Name the blood parasite species.
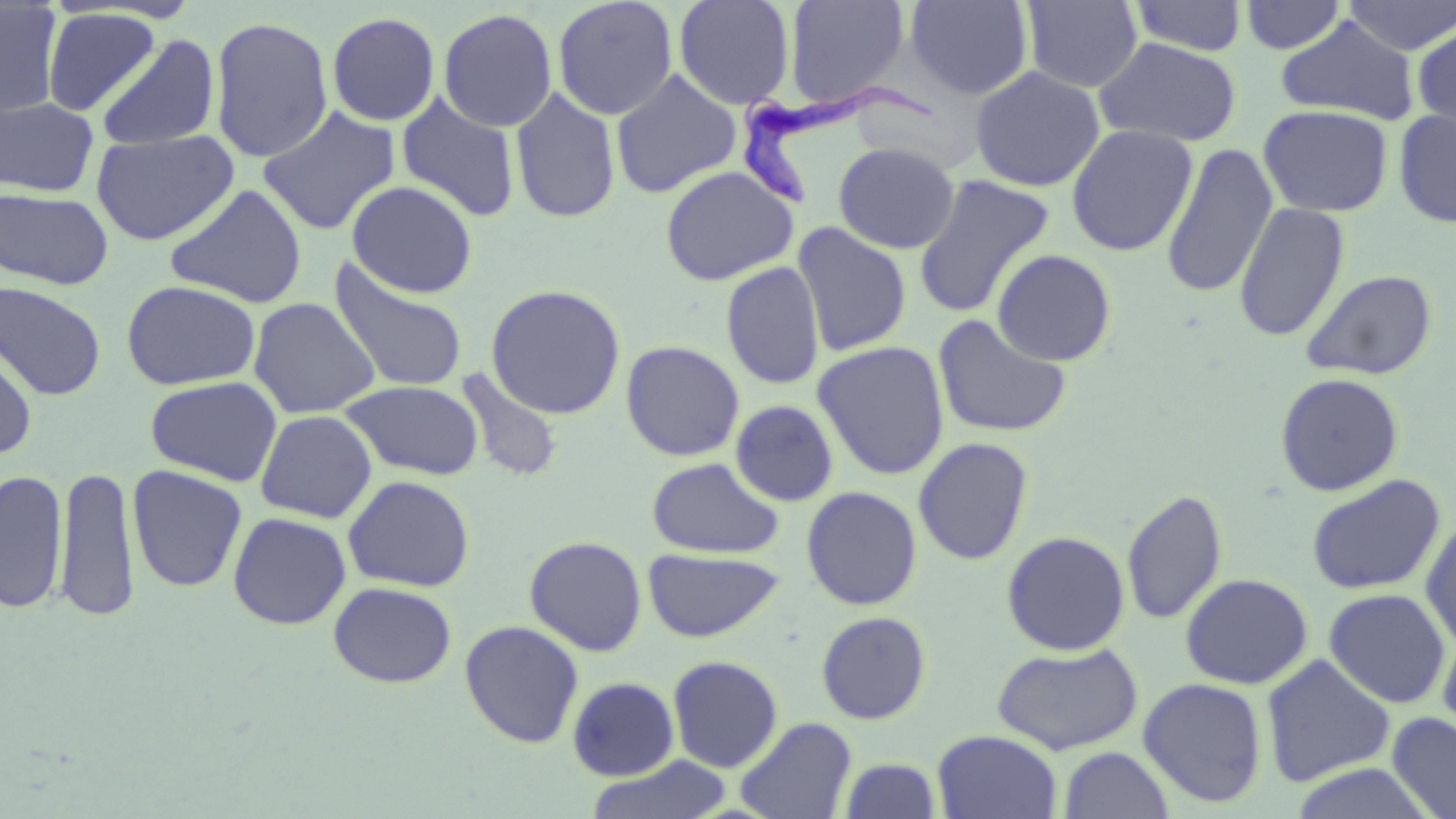
Trypanosoma brucei.

Approximate bounding boxes as named x1/y1/x2/y2 corners in pixels. Uninfected red blood cell locations: (x1=673, y1=0, x2=796, y2=110), (x1=905, y1=0, x2=1034, y2=100), (x1=1238, y1=0, x2=1348, y2=54), (x1=1339, y1=0, x2=1456, y2=55), (x1=552, y1=1, x2=678, y2=119), (x1=783, y1=1, x2=911, y2=110), (x1=1021, y1=1, x2=1143, y2=92), (x1=1128, y1=1, x2=1249, y2=56), (x1=0, y1=2, x2=64, y2=118), (x1=41, y1=8, x2=160, y2=116), (x1=438, y1=9, x2=558, y2=132), (x1=326, y1=12, x2=441, y2=126), (x1=209, y1=15, x2=334, y2=163), (x1=1275, y1=15, x2=1421, y2=124), (x1=1412, y1=19, x2=1456, y2=134), (x1=96, y1=33, x2=220, y2=151), (x1=1093, y1=36, x2=1243, y2=147), (x1=969, y1=66, x2=1105, y2=192), (x1=610, y1=69, x2=741, y2=199), (x1=510, y1=86, x2=621, y2=224), (x1=396, y1=93, x2=520, y2=222), (x1=0, y1=97, x2=98, y2=197), (x1=1258, y1=104, x2=1394, y2=217), (x1=257, y1=105, x2=401, y2=236), (x1=1393, y1=108, x2=1456, y2=228), (x1=1065, y1=124, x2=1198, y2=256), (x1=91, y1=129, x2=239, y2=245), (x1=833, y1=141, x2=960, y2=253), (x1=1160, y1=141, x2=1278, y2=299), (x1=659, y1=165, x2=798, y2=286), (x1=912, y1=174, x2=1055, y2=318), (x1=346, y1=180, x2=478, y2=298), (x1=164, y1=183, x2=308, y2=308), (x1=0, y1=188, x2=114, y2=290), (x1=1233, y1=201, x2=1350, y2=342), (x1=793, y1=221, x2=912, y2=357), (x1=992, y1=248, x2=1117, y2=366), (x1=329, y1=259, x2=469, y2=394), (x1=721, y1=261, x2=825, y2=390), (x1=1300, y1=268, x2=1438, y2=380), (x1=121, y1=280, x2=261, y2=390), (x1=0, y1=281, x2=107, y2=400), (x1=486, y1=284, x2=626, y2=419), (x1=248, y1=297, x2=380, y2=418), (x1=932, y1=314, x2=1073, y2=439), (x1=0, y1=336, x2=37, y2=459), (x1=620, y1=340, x2=745, y2=461), (x1=812, y1=340, x2=950, y2=480), (x1=456, y1=369, x2=565, y2=484), (x1=1274, y1=372, x2=1405, y2=496), (x1=145, y1=376, x2=283, y2=487), (x1=340, y1=380, x2=485, y2=480), (x1=730, y1=399, x2=839, y2=507), (x1=254, y1=409, x2=378, y2=523), (x1=913, y1=436, x2=1034, y2=565), (x1=646, y1=457, x2=784, y2=559), (x1=54, y1=464, x2=140, y2=622), (x1=127, y1=465, x2=248, y2=593), (x1=1, y1=467, x2=68, y2=614), (x1=1306, y1=473, x2=1446, y2=595), (x1=343, y1=475, x2=475, y2=592), (x1=801, y1=486, x2=923, y2=610), (x1=1122, y1=488, x2=1228, y2=626), (x1=228, y1=512, x2=351, y2=630), (x1=1420, y1=516, x2=1456, y2=653), (x1=1001, y1=530, x2=1130, y2=655), (x1=524, y1=535, x2=647, y2=656), (x1=643, y1=548, x2=784, y2=642), (x1=1180, y1=573, x2=1313, y2=689), (x1=328, y1=581, x2=457, y2=688), (x1=1324, y1=588, x2=1451, y2=708), (x1=815, y1=610, x2=932, y2=725), (x1=459, y1=620, x2=584, y2=748), (x1=1437, y1=629, x2=1456, y2=739), (x1=991, y1=641, x2=1144, y2=754), (x1=1260, y1=654, x2=1396, y2=787), (x1=668, y1=655, x2=783, y2=772), (x1=567, y1=676, x2=679, y2=781), (x1=1137, y1=677, x2=1268, y2=808), (x1=1387, y1=712, x2=1456, y2=819), (x1=735, y1=716, x2=857, y2=819), (x1=932, y1=730, x2=1063, y2=819), (x1=1057, y1=746, x2=1175, y2=819), (x1=583, y1=755, x2=734, y2=819), (x1=838, y1=758, x2=942, y2=818). Trypanosoma brucei locations: (x1=732, y1=79, x2=937, y2=208). Optical microscopy. Single field of view. Captured at 1000x magnification. Thin blood film. May-Grünwald-Giemsa stain. Image is 1456×819 pixels.